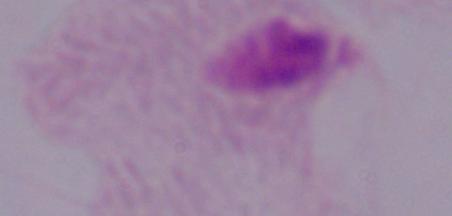

Captured at 1000x magnification. Photomicrograph. A trichomonad is seen.